Locate and identify every blood parasite.
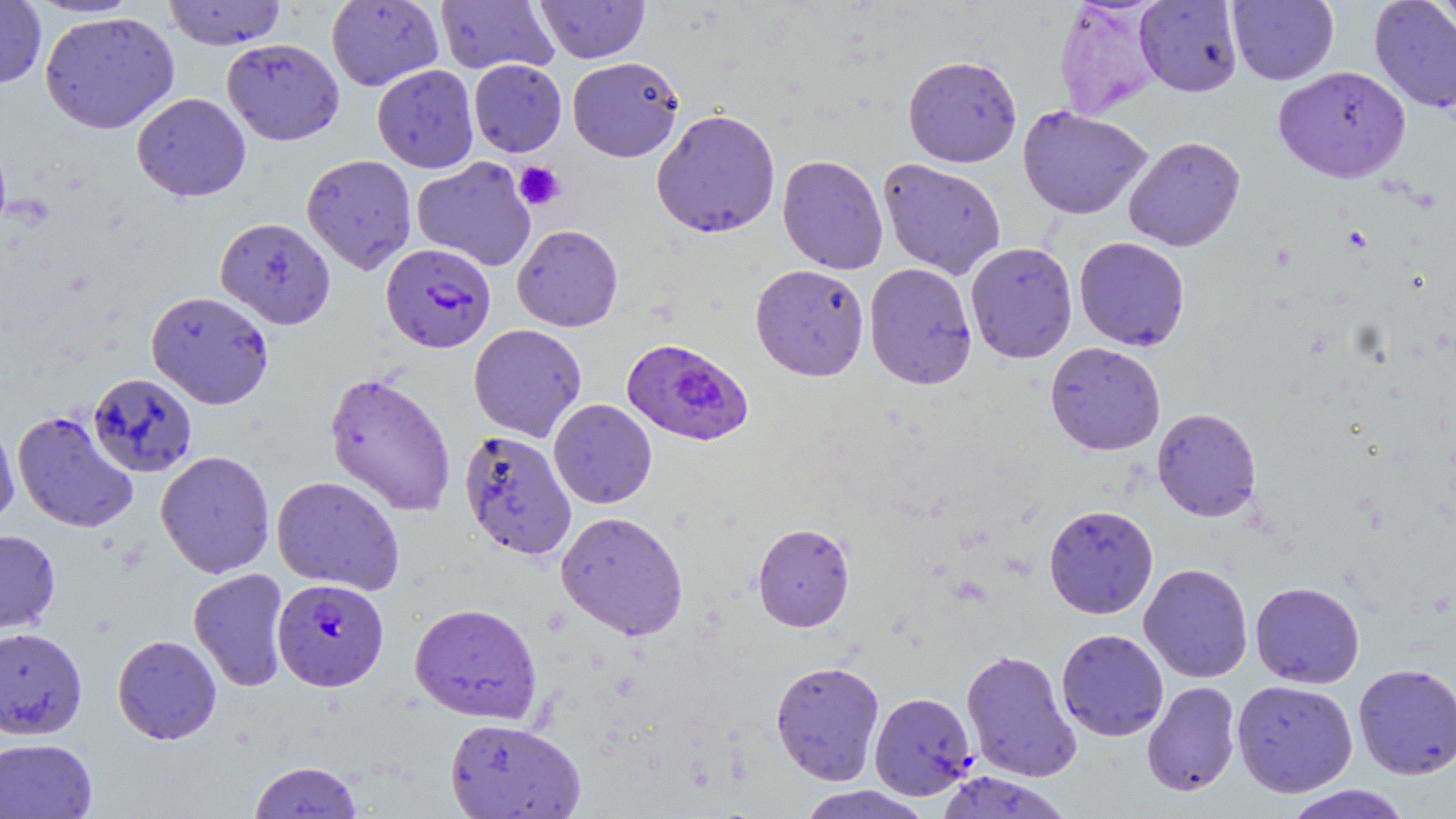

Approximate bounding boxes as [x1, y1, x2, y2] in pixels.
Plasmodium falciparum-infected red blood cells: [381, 243, 496, 353], [621, 337, 753, 447], [12, 410, 139, 534], [273, 577, 389, 691].
No Plasmodium ovale, Plasmodium malariae, Plasmodium vivax, Babesia divergens, or Trypanosoma brucei observed.

slide_level_diagnosis: Plasmodium falciparum
image_size: 1456×819 pixels
preparation: thin blood film
modality: light microscopy
magnification: 1000x
field_of_view: one of a larger specimen
uninfected_red_blood_cell_locations: 'approximate bounding boxes as [x1, y1, x2, y2] in pixels: [0, 0, 47, 88], [163, 0, 287, 50], [435, 0, 558, 75], [535, 0, 650, 64], [1227, 0, 1339, 85], [1368, 0, 1456, 113], [1430, 0, 1456, 39], [26, 1, 144, 18], [326, 1, 444, 91], [1135, 1, 1242, 97], [39, 11, 180, 134], [222, 38, 344, 145], [903, 55, 1022, 167], [567, 56, 684, 162], [468, 59, 567, 157], [372, 64, 479, 173], [1273, 65, 1411, 183], [132, 92, 251, 202], [1017, 105, 1152, 220], [651, 108, 781, 238], [1123, 135, 1246, 251], [301, 153, 417, 275], [777, 154, 888, 274], [412, 157, 537, 271], [878, 158, 1007, 279], [215, 217, 337, 330], [511, 224, 623, 332], [1074, 236, 1190, 351], [965, 241, 1078, 363], [863, 262, 977, 390], [750, 264, 869, 381], [146, 290, 273, 409], [468, 323, 587, 442], [1045, 341, 1166, 455], [324, 370, 457, 517], [87, 372, 198, 477], [549, 398, 657, 509], [1151, 406, 1262, 522], [0, 415, 19, 529], [459, 429, 577, 561], [155, 450, 275, 578], [271, 475, 405, 595], [1043, 503, 1159, 619], [556, 510, 688, 640], [752, 522, 855, 632], [0, 528, 60, 634], [1139, 562, 1253, 683], [188, 568, 291, 692], [1250, 581, 1365, 688], [409, 602, 542, 724], [0, 626, 87, 739], [1056, 628, 1169, 741], [112, 634, 222, 744], [961, 649, 1082, 783], [770, 660, 885, 785], [1353, 662, 1456, 779], [1232, 678, 1358, 797], [1142, 681, 1241, 797], [869, 691, 977, 800], [444, 718, 586, 818], [0, 737, 97, 818], [248, 761, 362, 819], [934, 771, 1073, 818], [796, 785, 932, 819], [1282, 785, 1413, 819]'
platelet_locations: 'approximate bounding boxes as [x1, y1, x2, y2] in pixels: [514, 162, 565, 210]'
stain: May-Grünwald-Giemsa